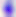

magnification: 400x
identification: Toxoplasma gondii
modality: photomicrograph